Assess the morphology of the red blood cells.
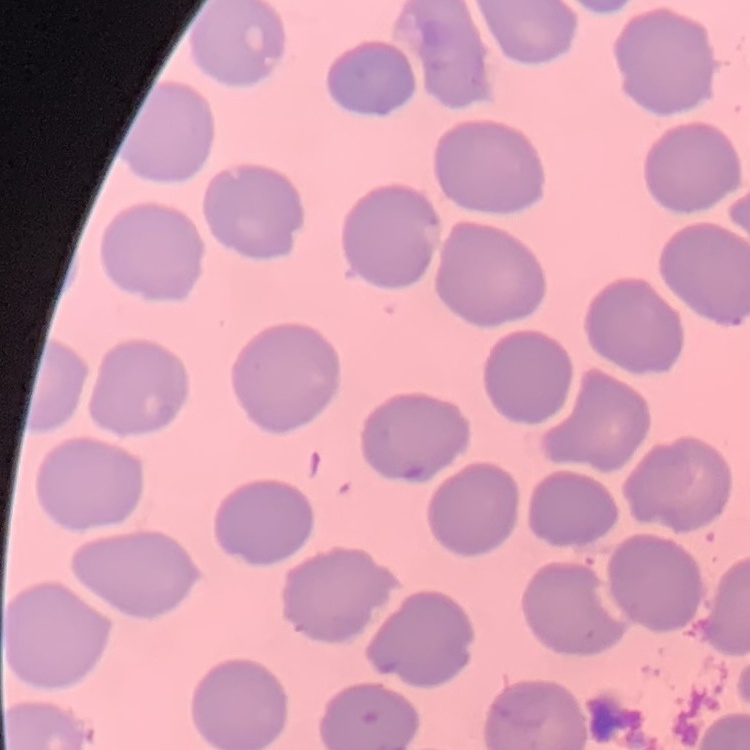
No rouleaux formation.

Stained with either Field's or Giemsa. Thin peripheral smear. One tile cut from a larger photomicrograph.